Evaluate for Plasmodium parasites.
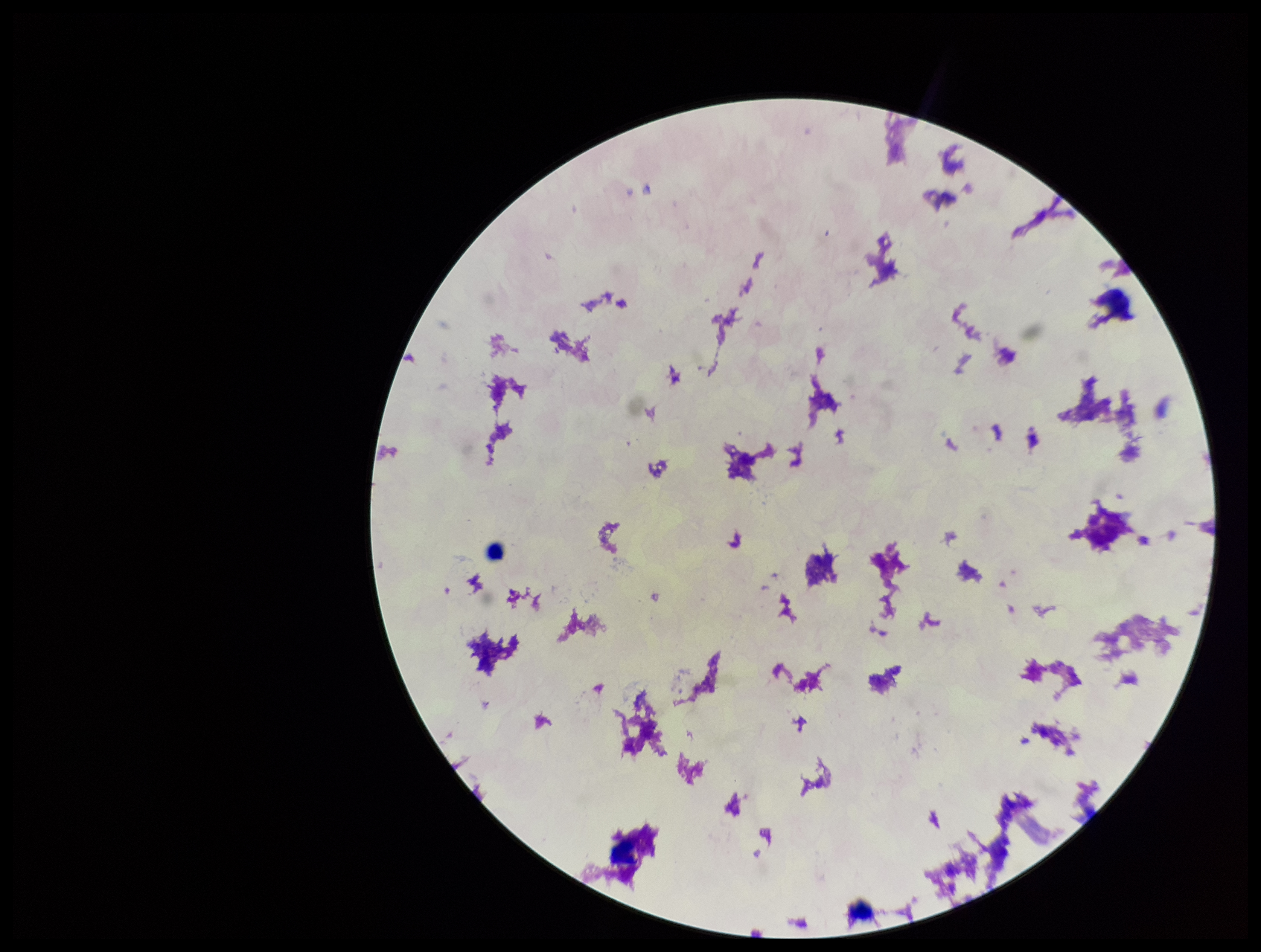
None detected.

Photographed through the microscope eyepiece with a smartphone camera. Image is 1261×952 pixels. Giemsa stain. Patient malaria status: negative. Leukocyte count: 3. Parasite count: 0. One field from this slide. Preparation: thick smear.